Assess this cell for malaria.
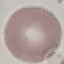
It is uninfected.

image type = automatically extracted cell patch, resized to 64 × 64 pixels
capture = smartphone through the microscope eyepiece
preparation = thin blood film
stain = Giemsa